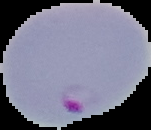
Image is 151×130 pixels. The area outside the segmented cell region is set to black. From a thin blood film. Malaria status: parasitized.